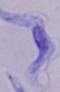

Summary:
  - Magnification: 1000x
  - Identification: trypanosome
  - Modality: photomicrograph